Give the extent of all Plasmodium ovale-infected red blood cells.
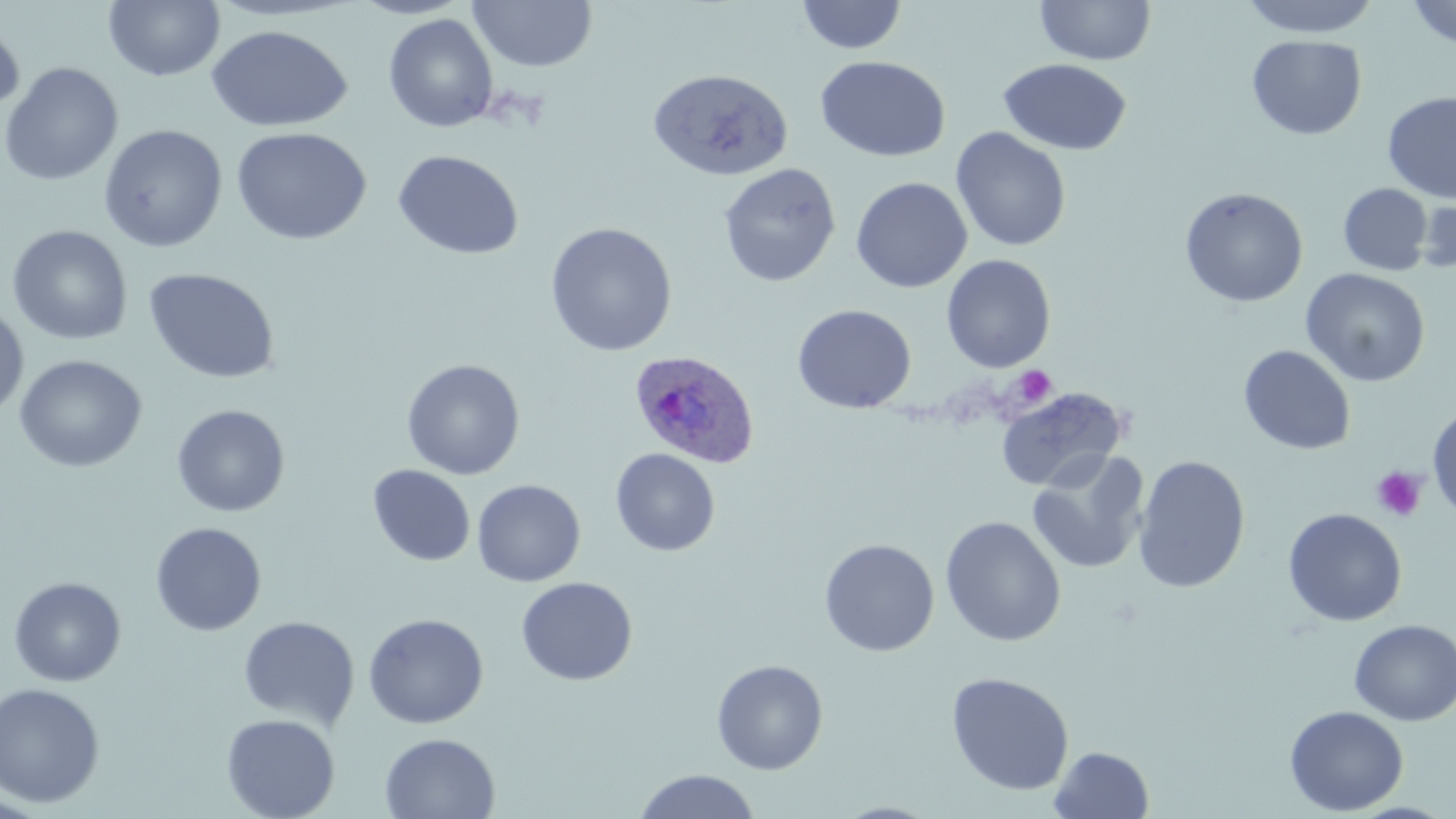

Approximate bounding boxes as (x1,y1)-(x2,y2) corner pairs in pixels.
Plasmodium ovale-infected red blood cells: (628,349)-(761,470).

Summary:
  - Uninfected red blood cell locations: (104,0)-(225,82), (467,0)-(598,73), (796,0)-(908,54), (1238,0)-(1384,38), (1407,0)-(1456,48), (1035,1)-(1156,66), (384,13)-(499,133), (0,17)-(24,120), (206,25)-(352,132), (1247,34)-(1367,140), (815,55)-(951,162), (998,58)-(1132,156), (0,62)-(124,186), (647,67)-(793,181), (1382,91)-(1456,203), (99,125)-(228,253), (231,127)-(372,245), (951,127)-(1071,252), (392,149)-(524,260), (718,163)-(841,288), (850,176)-(973,293), (1338,183)-(1433,276), (1179,187)-(1308,307), (1412,197)-(1456,276), (544,222)-(678,356), (6,225)-(133,345), (941,254)-(1056,372), (143,267)-(280,384), (1301,268)-(1430,388), (792,303)-(916,414), (0,305)-(29,419), (1238,345)-(1356,455), (14,354)-(148,473), (401,359)-(525,480), (995,387)-(1127,493), (171,404)-(290,517), (1426,405)-(1456,522), (610,448)-(720,556), (1026,449)-(1151,575), (1133,455)-(1251,593), (368,464)-(475,566), (472,479)-(586,587), (1283,508)-(1407,627), (940,516)-(1066,647), (150,522)-(267,636), (819,538)-(940,656), (8,576)-(126,687), (516,576)-(638,686), (363,613)-(489,729), (238,616)-(360,732), (1349,619)-(1455,726), (711,659)-(829,775), (946,671)-(1074,796), (0,683)-(105,808), (1284,705)-(1408,815), (221,713)-(340,819), (379,733)-(501,819), (1048,746)-(1155,819), (633,769)-(762,819)
  - Platelet locations: (1011,366)-(1057,408), (1372,465)-(1428,522)
  - Slide-level diagnosis: Plasmodium ovale
  - Preparation: thin blood film
  - Magnification: 1000x
  - Modality: optical microscopy
  - Field of view: one of a larger specimen
  - Image size: 1456×819 pixels
  - Stain: May-Grünwald-Giemsa